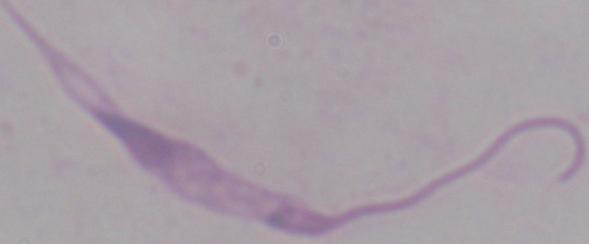

magnification = 1000x
modality = micrograph
identification = Leishmania